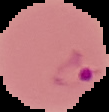

Summary:
  - Image size: 109×112 pixels
  - Preparation: thin blood smear
  - Result: Plasmodium parasites detected
  - Image type: segmented cell region on a black background